Assess this cell for malaria.
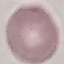

Uninfected.

Summary:
  - Image type: automatically extracted cell patch, resized to 64 × 64 pixels
  - Preparation: thin blood film
  - Capture: smartphone through the microscope eyepiece
  - Stain: Giemsa